Comment on the morphology of the erythrocytes.
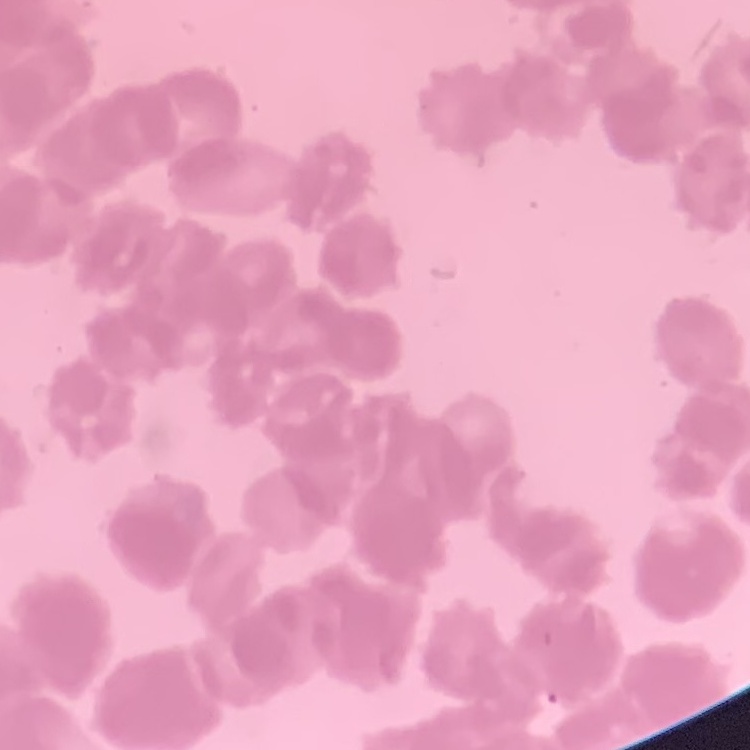

They show rouleaux formation.

preparation = thin blood smear
image type = one tile cut from a larger photomicrograph
stain = Field's or Giemsa